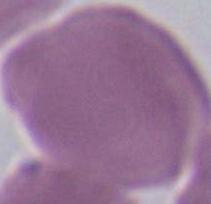
Summary:
  - Magnification: 1000x
  - Modality: micrograph
  - Identification: red blood cell